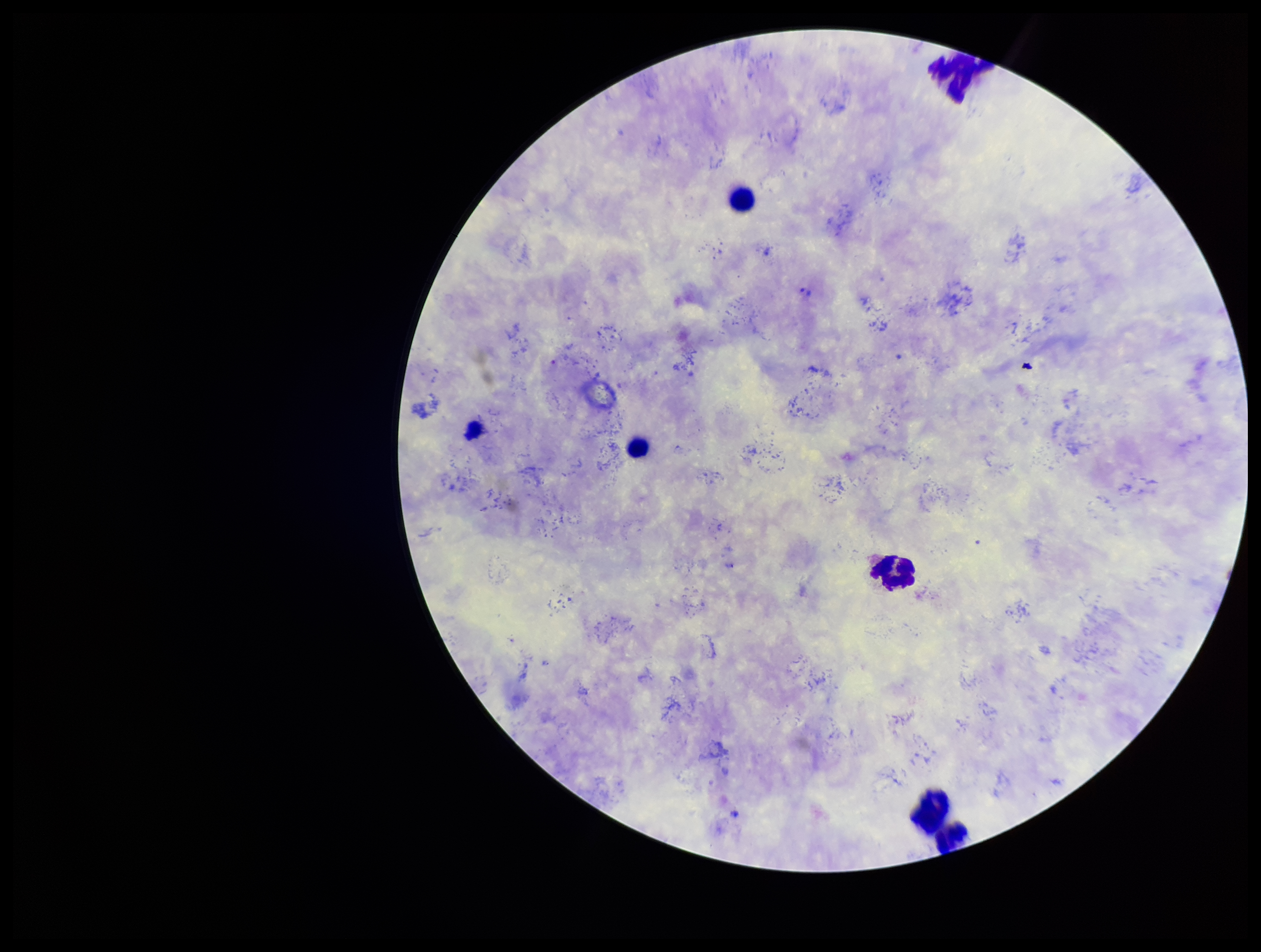
Smartphone photograph taken through the eyepiece of a microscope. Patient malaria status: infected. Image is 1261×952 pixels. One field from this slide. Species reported for this patient: Plasmodium vivax. Plasmodium parasites: none identified. Giemsa stain. Leukocyte count: 6. Preparation: thick blood smear. Parasite count: 0.